Give the position of every Plasmodium parasite.
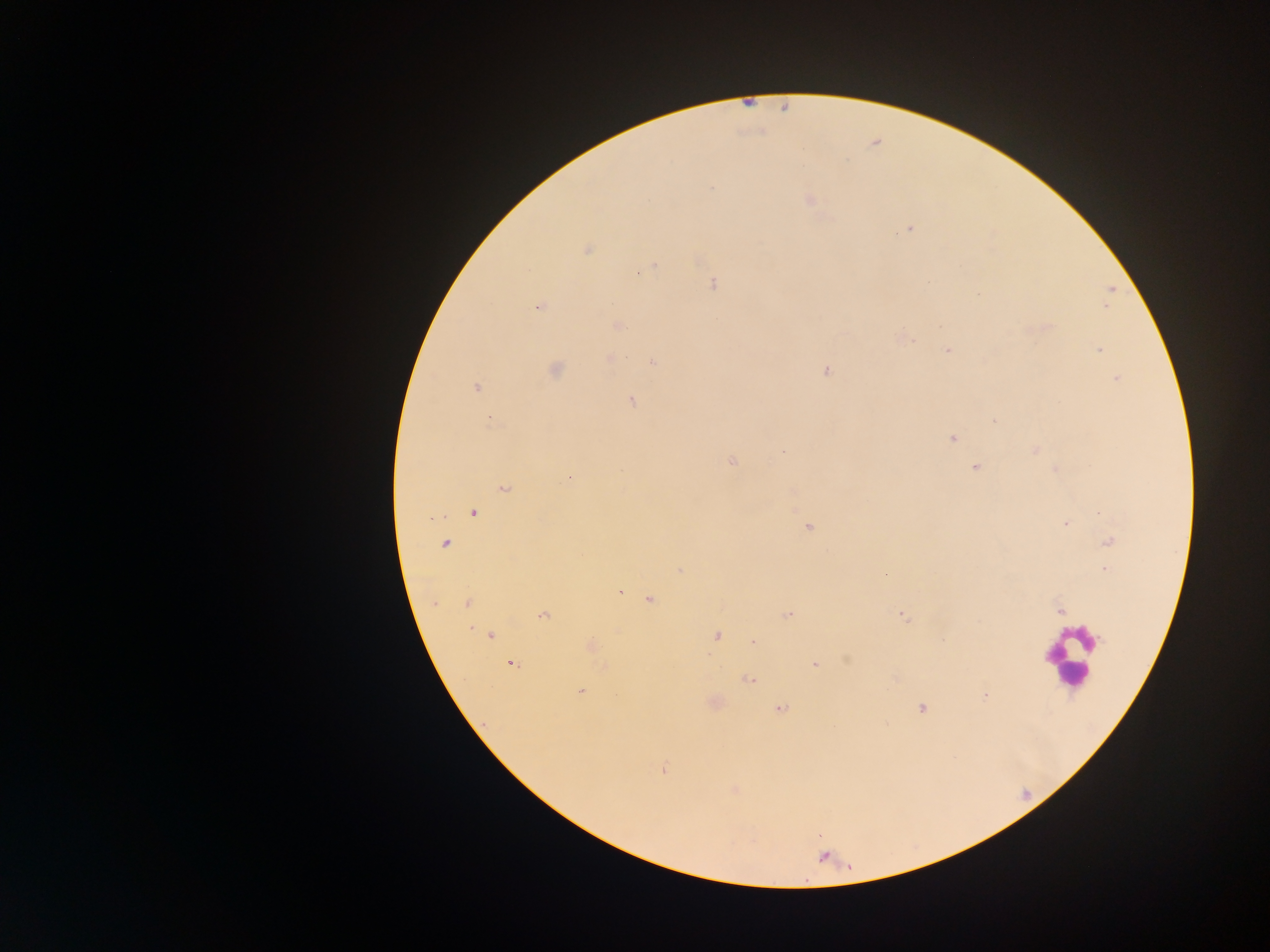
Approximate centers as {x, y} in pixels.
Plasmodium parasites: {711, 188}, {810, 200}, {909, 228}, {587, 250}, {652, 265}, {639, 271}, {713, 283}, {1111, 290}, {979, 294}, {1110, 298}, {539, 306}, {1107, 307}, {617, 325}, {1047, 327}, {904, 338}, {947, 350}, {1098, 350}, {609, 359}, {653, 362}, {555, 370}, {827, 372}, {1117, 379}, {476, 388}, {630, 401}, {993, 421}, {489, 422}, {952, 438}, {783, 451}, {1035, 451}, {732, 462}, {975, 468}, {570, 477}, {503, 489}, {474, 512}, {1065, 524}, {809, 527}, {1109, 541}, {445, 543}, {679, 570}, {1105, 570}, {886, 573}, {620, 593}, {649, 600}, {467, 604}, {1060, 610}, {543, 614}, {788, 614}, {903, 616}, {469, 628}, {490, 636}, {717, 636}, {942, 640}, {753, 642}, {591, 646}, {512, 663}, {814, 665}, {605, 668}, {748, 680}, {581, 691}, {985, 696}, {781, 708}, {922, 708}, {663, 769}.

{
  "preparation": "thick blood film",
  "leukocyte_locations": "approximate centers as {x, y} in pixels: {1069, 658}",
  "capture": "mobile-phone photograph through a microscope",
  "field_of_view": "single",
  "image_size": "1270×952 pixels",
  "country": "Ghana"
}